Give the extent of all Plasmodium falciparum-infected red blood cells.
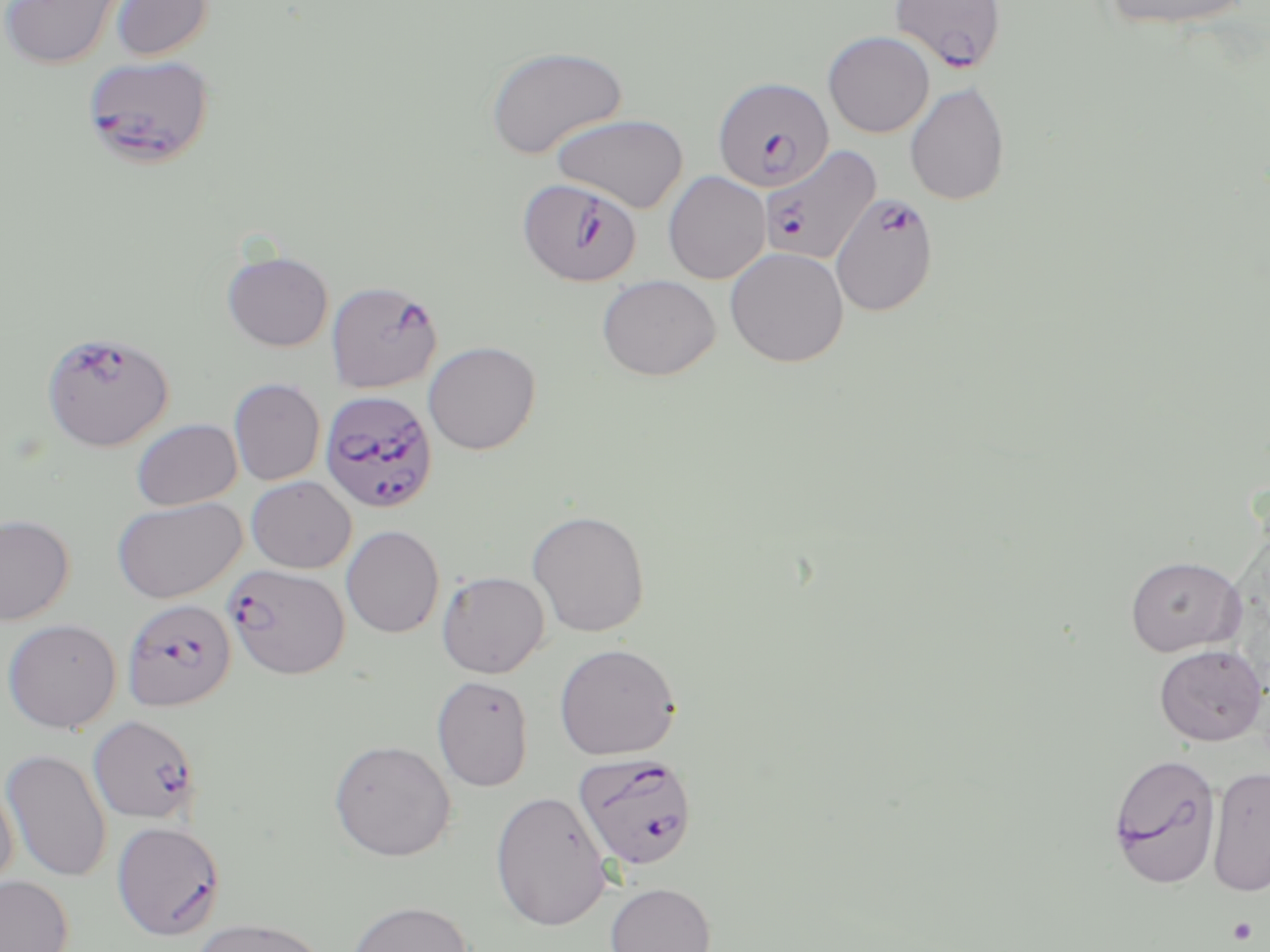
Approximate bounding boxes as (x1, y1, x2, y2) in pixels.
Plasmodium falciparum-infected red blood cells (subset): (890, 0, 1006, 74), (83, 54, 216, 167), (713, 76, 834, 193), (760, 146, 883, 266), (518, 177, 642, 287), (830, 192, 939, 316), (326, 280, 443, 393), (41, 330, 175, 452), (319, 389, 439, 513), (121, 598, 236, 711), (573, 752, 699, 871), (1108, 753, 1222, 888), (111, 821, 225, 941).

slide-level diagnosis = Plasmodium falciparum
modality = optical microscopy
image size = 1270×952 pixels
field of view = one of a larger specimen
uninfected red blood cell locations (subset) = approximate bounding boxes as (x1, y1, x2, y2) in pixels: (0, 0, 124, 70), (108, 0, 214, 62), (1099, 0, 1256, 31), (822, 30, 935, 138), (485, 45, 628, 160), (904, 82, 1011, 206), (552, 114, 689, 213), (662, 171, 771, 284), (724, 246, 849, 367), (221, 250, 333, 351), (597, 274, 721, 380), (423, 341, 541, 455), (228, 378, 326, 485), (132, 418, 242, 511), (246, 476, 356, 573), (112, 497, 245, 603), (526, 509, 651, 638), (0, 513, 75, 625), (341, 525, 444, 638), (1125, 555, 1246, 656), (437, 570, 550, 678), (1, 618, 121, 733), (553, 642, 681, 760), (1154, 644, 1267, 746), (431, 675, 534, 791), (328, 739, 457, 861), (2, 748, 112, 882), (1207, 765, 1270, 896), (0, 773, 19, 892), (490, 790, 613, 931), (1, 875, 73, 952), (606, 882, 716, 952), (344, 899, 474, 952), (187, 917, 332, 952)
preparation = thin blood film
magnification = 1000x
stain = May-Grünwald-Giemsa
platelet locations = approximate bounding boxes as (x1, y1, x2, y2) in pixels: (1228, 917, 1257, 944)